Report the malaria status of this cell.
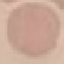
Uninfected.

Giemsa stain. Cell patch, automatically extracted from a larger field of view and resized to 64 × 64 pixels. Thin smear of blood. Acquired by smartphone through the microscope eyepiece.